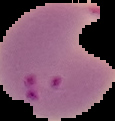
Summary:
  - Malaria status: parasitized
  - Image type: segmented cell region with the area outside set to black
  - Image size: 115×121 pixels
  - Preparation: thin blood film